Describe the morphology of the red blood cells.
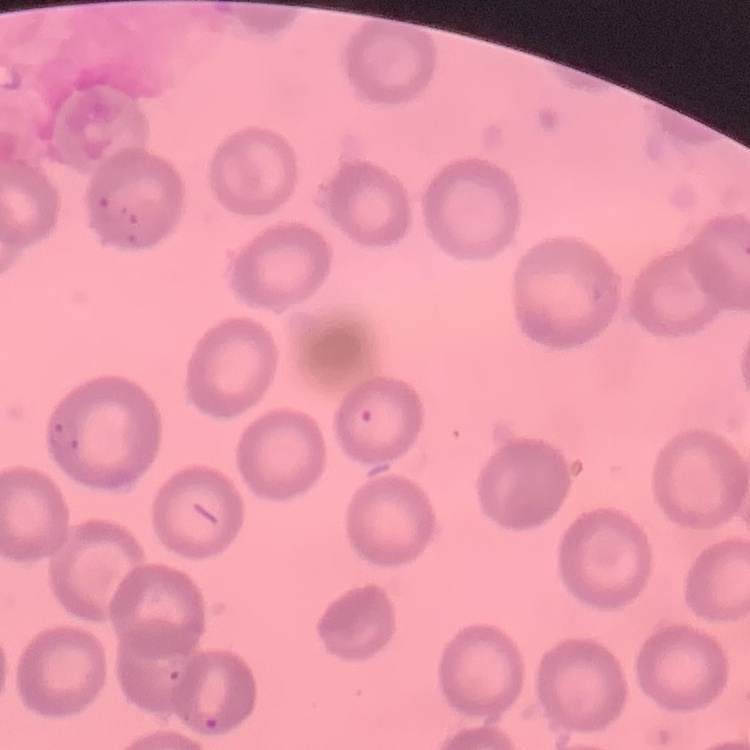

They show no rouleaux formation.

preparation = thin blood film
image type = square crop of a larger photomicrograph
stain = Field's or Giemsa